Assess the morphology of the erythrocytes.
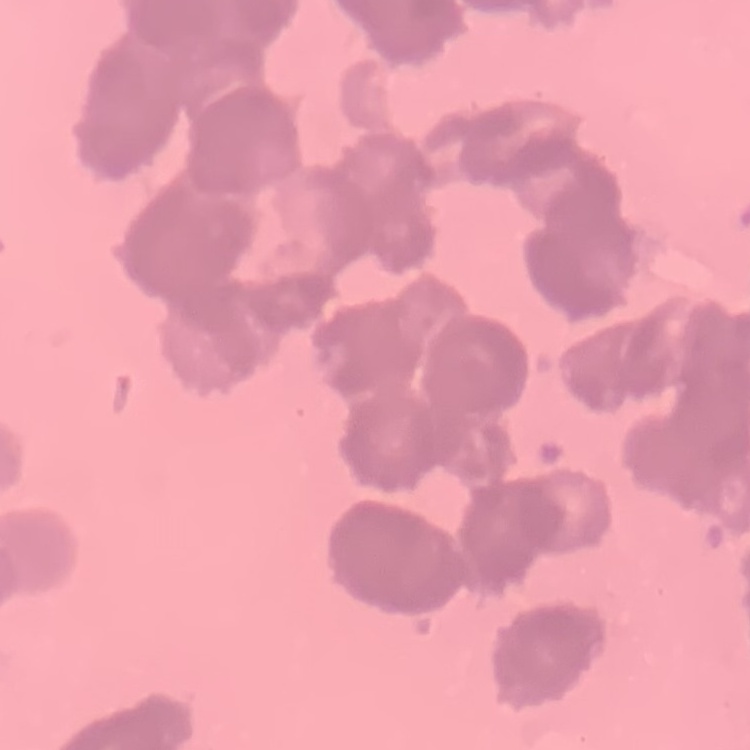
They show rouleaux formation.

{
  "stain": "Field's or Giemsa",
  "preparation": "thin blood film",
  "image_type": "square crop of a larger photomicrograph"
}